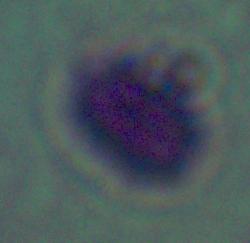
Summary:
  - Identification: Leishmania
  - Modality: micrograph
  - Magnification: 1000x